Locate every Plasmodium parasite.
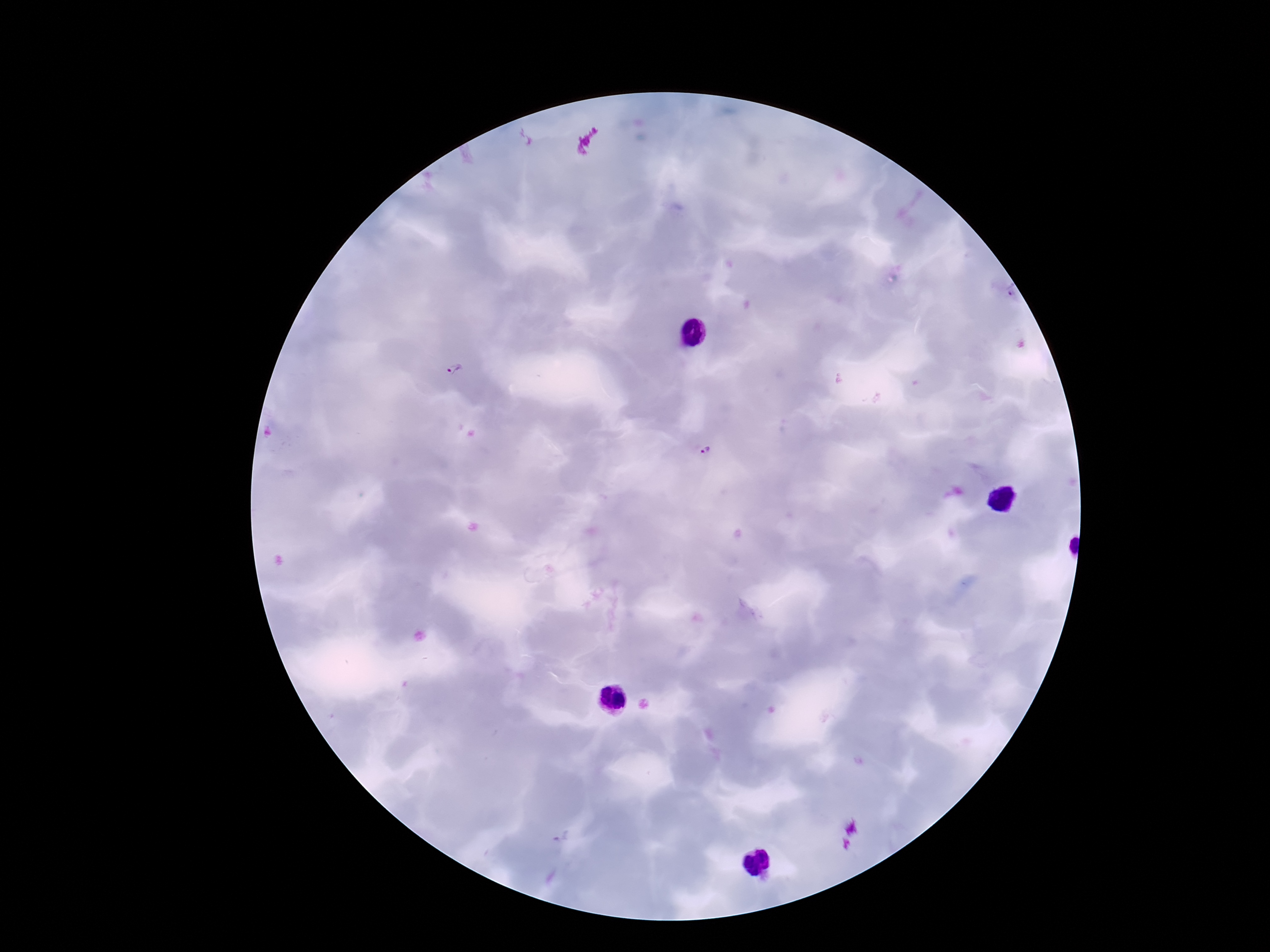
Approximate object centers, in pixels from the top-left corner.
Plasmodium parasites: (x=454, y=372), (x=704, y=451).

capture = smartphone camera through the microscope eyepiece
magnification = 100x
preparation = thick blood smear
stain = Giemsa
field of view = single
patient malaria status = positive
image size = 1270×952 pixels